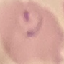

malaria status = parasitized
capture = smartphone through the microscope eyepiece
image type = automatically extracted cell patch, resized to 64 × 64 pixels
preparation = thin smear
stain = Giemsa